Locate every Plasmodium parasite.
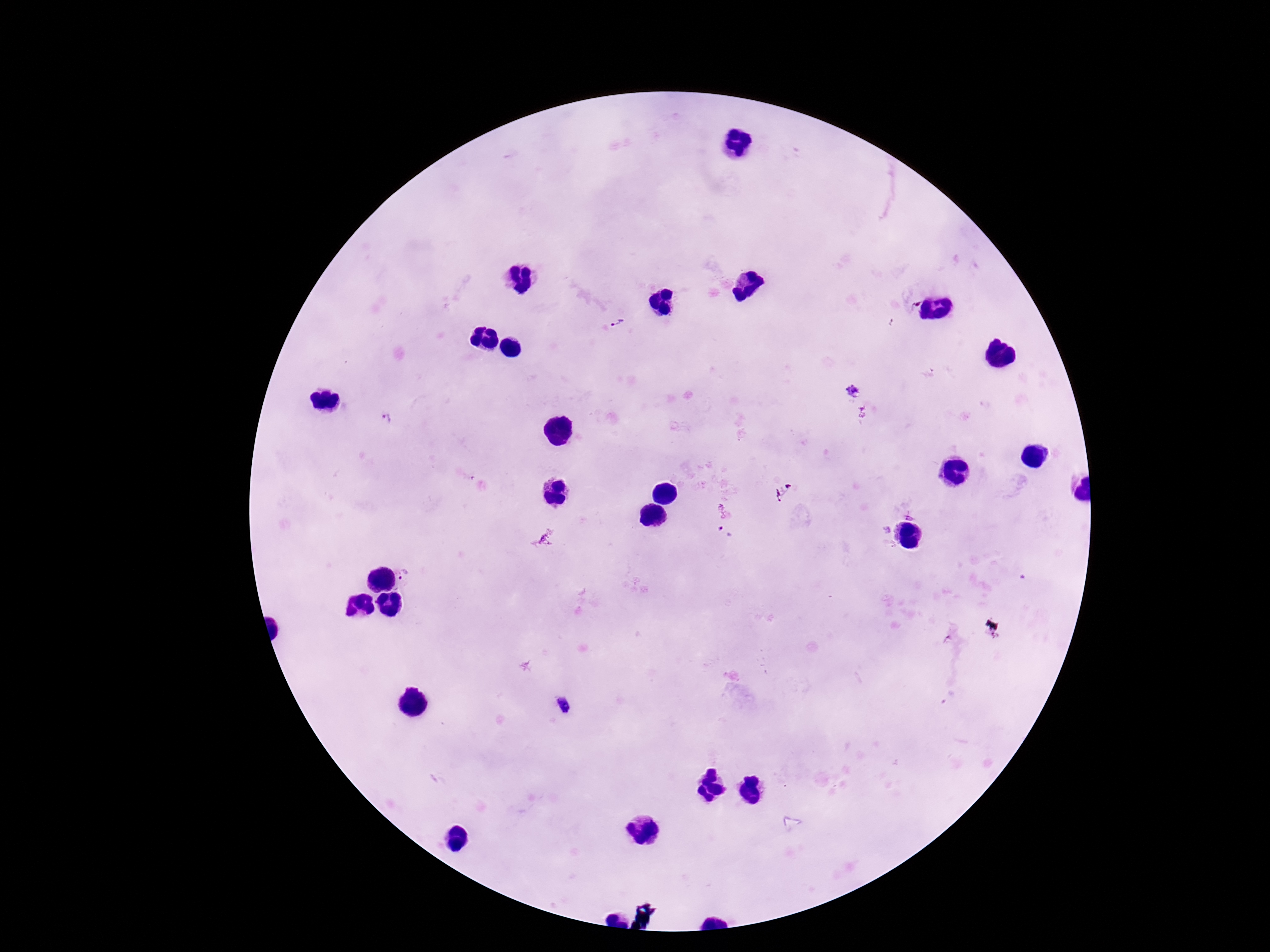

Approximate centers as [x, y] in pixels.
Plasmodium parasites: [913, 304], [616, 322], [854, 390], [861, 411], [387, 418], [724, 533], [407, 576].

Summary:
  - Field of view: single
  - Magnification: 100x
  - Capture: smartphone camera through the microscope eyepiece
  - Image size: 1270×952 pixels
  - Preparation: thick blood film
  - Patient malaria status: infected
  - Stain: Giemsa